Assess the morphology of the red blood cells.
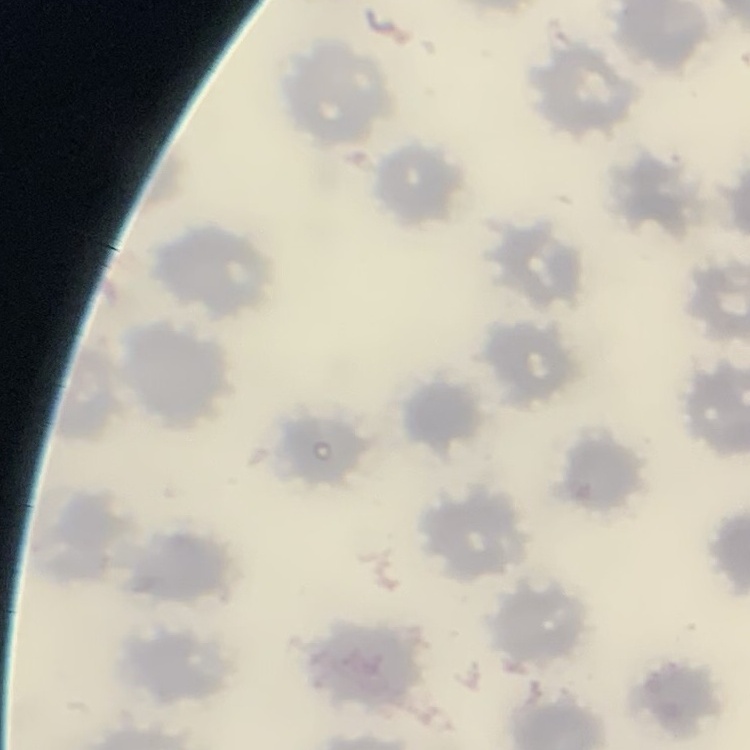

They show no rouleaux formation.

Stained with either Field's or Giemsa. Thin blood film. Square crop of a larger photomicrograph.